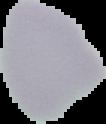

Summary:
  - Malaria status: uninfected
  - Image type: segmented cell region with the area outside set to black
  - Image size: 106×124 pixels
  - Preparation: thin blood smear